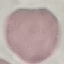 Result: negative for malaria parasites. Thin smear of blood. Cell patch, automatically extracted from a larger field of view and resized to 64 × 64 pixels. Photographed with a smartphone camera at the microscope eyepiece. Giemsa stain.